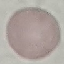
Malaria status: uninfected. Thin blood film. Giemsa-stained preparation. Automatically extracted cell patch, resized to 64 × 64 pixels. Acquired by smartphone through the microscope eyepiece.